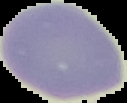

image type = cell region segmented out of the field of view; surrounding area masked to black
malaria status = uninfected
image size = 127×103 pixels
preparation = thin blood film